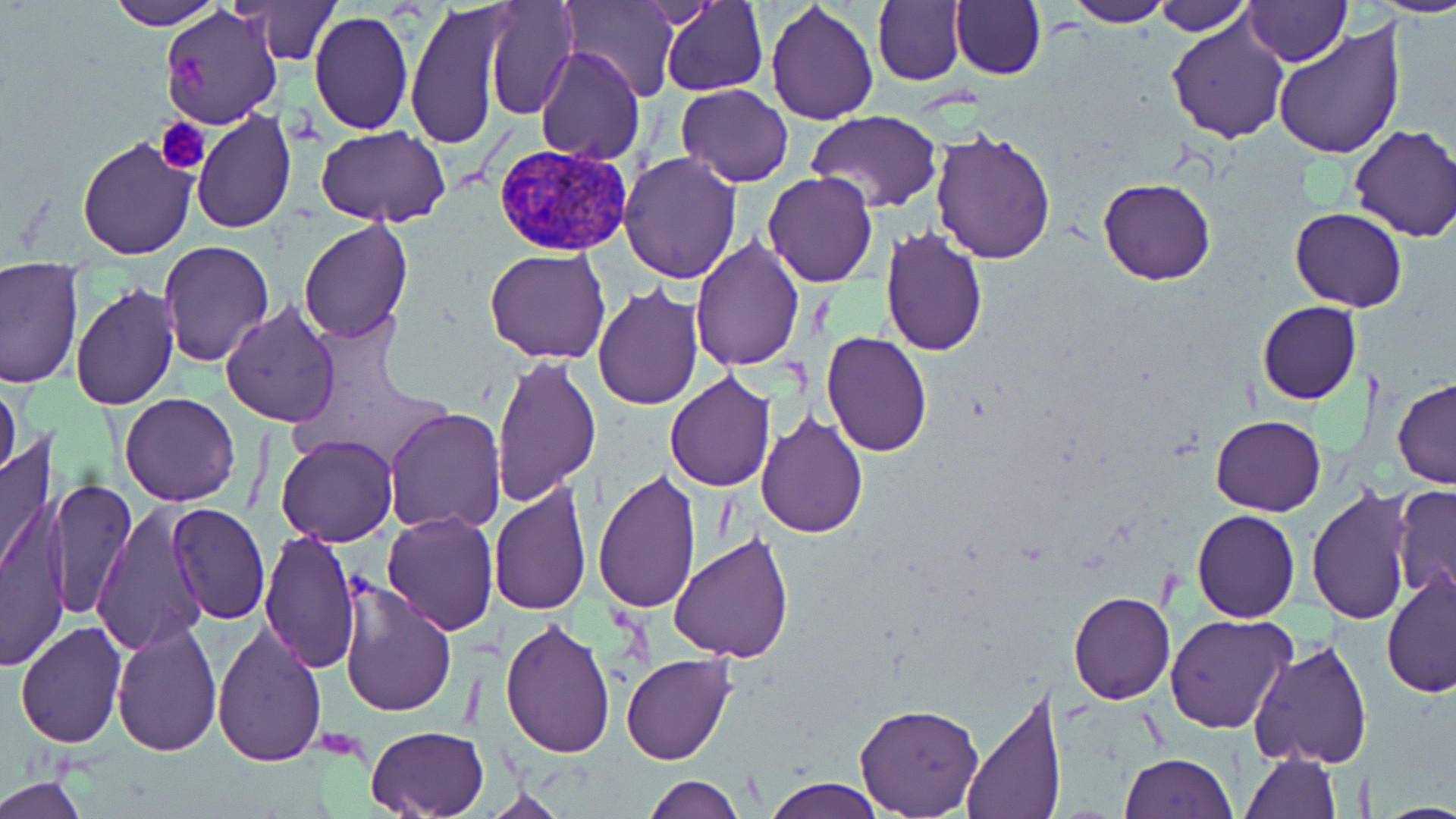
Summary:
  - Coordinate format: approximate bounding boxes as [x1, y1, x2, y2] in pixels
  - Plasmodium vivax-infected red blood cell locations: [493, 144, 633, 256]
  - Platelet locations: [173, 49, 213, 103], [156, 117, 209, 173]
  - Uninfected red blood cell locations: [104, 0, 218, 29], [245, 0, 339, 64], [483, 0, 576, 120], [562, 0, 679, 105], [661, 0, 767, 97], [950, 0, 1045, 81], [1061, 0, 1173, 27], [1153, 0, 1251, 35], [1245, 0, 1348, 66], [1379, 0, 1456, 16], [407, 1, 508, 150], [873, 1, 966, 86], [765, 2, 879, 126], [159, 5, 283, 128], [307, 9, 413, 135], [1167, 13, 1291, 141], [1272, 20, 1406, 161], [535, 46, 644, 164], [676, 84, 793, 186], [192, 108, 297, 231], [806, 110, 944, 214], [316, 126, 450, 227], [1348, 126, 1456, 242], [930, 128, 1057, 265], [76, 134, 201, 260], [618, 151, 742, 284], [763, 171, 877, 287], [1099, 178, 1215, 285], [1290, 208, 1408, 311], [298, 218, 415, 342], [880, 225, 988, 357], [689, 238, 805, 372], [157, 240, 274, 367], [485, 247, 611, 364], [0, 263, 82, 390], [69, 282, 181, 411], [593, 284, 703, 411], [1258, 300, 1361, 404], [221, 302, 342, 428], [822, 331, 933, 457], [490, 353, 602, 506], [664, 372, 775, 492], [0, 377, 22, 489], [1392, 379, 1456, 487], [120, 393, 242, 506], [384, 407, 506, 533], [757, 412, 867, 538], [1210, 415, 1327, 517], [0, 431, 57, 591], [276, 433, 397, 547], [591, 470, 704, 615], [49, 479, 134, 620], [489, 482, 591, 616], [1392, 485, 1456, 603], [1305, 487, 1414, 625], [2, 492, 73, 670], [168, 502, 270, 623], [90, 504, 212, 656], [1192, 510, 1299, 622], [382, 511, 498, 635], [258, 527, 362, 674], [668, 532, 795, 665], [1381, 571, 1456, 700], [338, 581, 457, 718], [1068, 591, 1176, 704], [1164, 613, 1297, 734], [498, 618, 616, 758], [112, 621, 223, 755], [211, 621, 327, 768], [15, 622, 126, 749], [1249, 639, 1372, 770], [621, 653, 736, 764], [959, 689, 1067, 819], [854, 703, 984, 816], [366, 725, 487, 816], [1240, 749, 1340, 819], [1119, 752, 1237, 819], [2, 776, 87, 819], [644, 776, 744, 818], [764, 777, 884, 818], [475, 789, 574, 818], [1376, 800, 1456, 818]
  - Slide-level diagnosis: Plasmodium vivax
  - Magnification: 1000x
  - Stain: May-Grünwald-Giemsa
  - Field of view: single
  - Image size: 1456×819 pixels
  - Modality: light microscopy
  - Preparation: thin blood smear